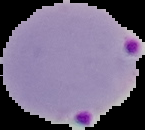

preparation = thin blood film
malaria status = parasitized
image size = 145×130 pixels
image type = cell region segmented out of the field of view; surrounding area masked to black